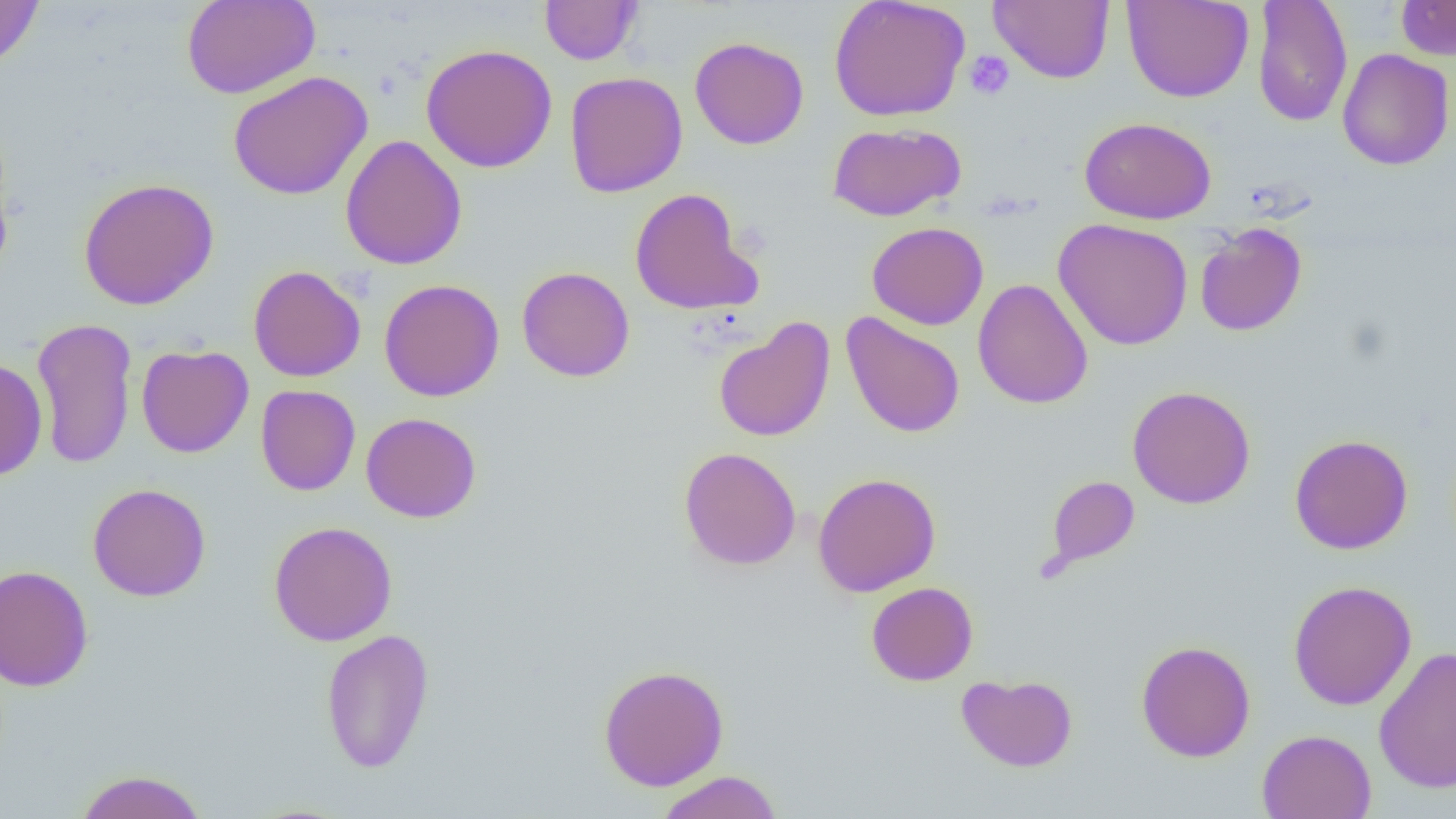 Approximate bounding boxes as named x1/y1/x2/y2 corners in pixels. Uninfected red blood cell locations: (x1=0, y1=0, x2=44, y2=71), (x1=182, y1=0, x2=320, y2=99), (x1=539, y1=0, x2=643, y2=66), (x1=829, y1=0, x2=970, y2=122), (x1=988, y1=0, x2=1115, y2=84), (x1=1122, y1=0, x2=1254, y2=103), (x1=1395, y1=0, x2=1456, y2=60), (x1=1252, y1=1, x2=1352, y2=128), (x1=689, y1=36, x2=809, y2=150), (x1=421, y1=44, x2=558, y2=173), (x1=1337, y1=48, x2=1454, y2=171), (x1=228, y1=70, x2=373, y2=200), (x1=565, y1=71, x2=688, y2=197), (x1=1079, y1=116, x2=1217, y2=224), (x1=827, y1=122, x2=965, y2=222), (x1=340, y1=134, x2=467, y2=271), (x1=78, y1=177, x2=219, y2=311), (x1=629, y1=187, x2=761, y2=315), (x1=1053, y1=218, x2=1193, y2=351), (x1=866, y1=221, x2=989, y2=329), (x1=1194, y1=222, x2=1308, y2=337), (x1=248, y1=264, x2=366, y2=382), (x1=517, y1=266, x2=635, y2=382), (x1=972, y1=278, x2=1093, y2=409), (x1=379, y1=279, x2=504, y2=401), (x1=841, y1=312, x2=965, y2=438), (x1=31, y1=316, x2=138, y2=470), (x1=713, y1=316, x2=836, y2=443), (x1=136, y1=344, x2=254, y2=458), (x1=0, y1=358, x2=47, y2=482), (x1=256, y1=384, x2=361, y2=496), (x1=1127, y1=385, x2=1255, y2=508), (x1=361, y1=411, x2=482, y2=523), (x1=1289, y1=434, x2=1413, y2=555), (x1=678, y1=447, x2=801, y2=570), (x1=812, y1=473, x2=941, y2=597), (x1=1046, y1=474, x2=1140, y2=570), (x1=87, y1=483, x2=211, y2=601), (x1=268, y1=521, x2=398, y2=646), (x1=0, y1=564, x2=94, y2=691), (x1=1287, y1=580, x2=1417, y2=711), (x1=866, y1=581, x2=978, y2=686), (x1=320, y1=628, x2=435, y2=773), (x1=1135, y1=640, x2=1256, y2=762), (x1=1373, y1=646, x2=1456, y2=793), (x1=598, y1=664, x2=729, y2=791), (x1=956, y1=673, x2=1078, y2=772), (x1=1257, y1=729, x2=1377, y2=819), (x1=74, y1=769, x2=209, y2=819), (x1=655, y1=770, x2=783, y2=819). Platelet locations: (x1=964, y1=50, x2=1015, y2=100). Slide-level diagnosis: no evidence of blood parasites. Captured at 1000x magnification. Single field of view. Thin blood film. Light microscopy. Image is 1456×819 pixels.